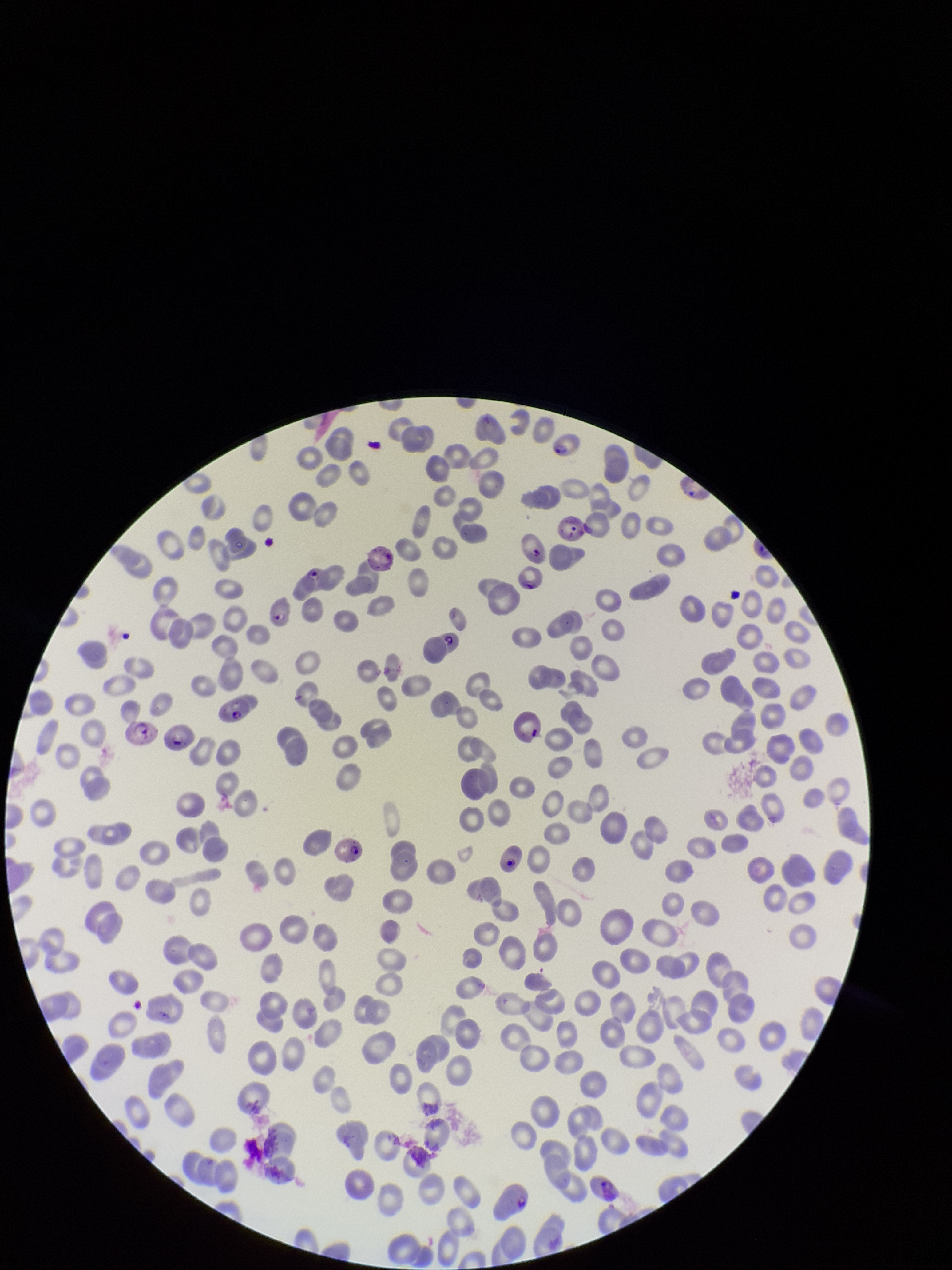

Summary:
  - Stain: Giemsa
  - Species reported for this patient: Plasmodium falciparum
  - Parasitized red blood cell count: 16
  - Capture: smartphone photograph through the microscope eyepiece
  - Image size: 952×1270 pixels
  - Patient malaria status: infected
  - Field of view: one from this slide
  - Preparation: thin blood smear
  - Parasitized red blood cells: seen
  - Red blood cell count: 258